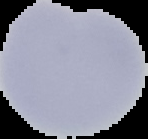

image type = segmented cell region on a black background
result = no Plasmodium parasites seen
image size = 148×139 pixels
preparation = thin blood smear